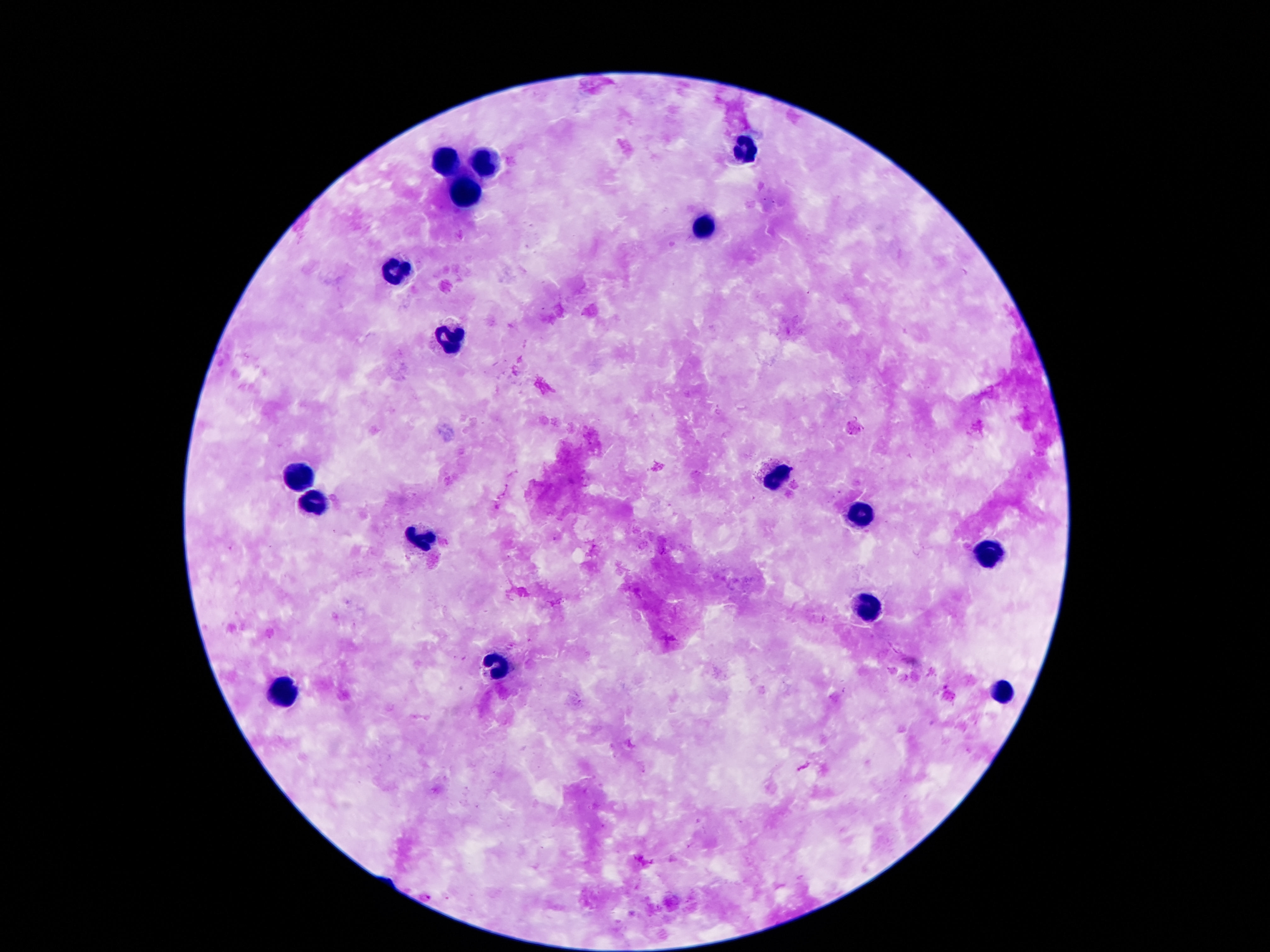

Approximate object centers, in pixels from the top-left corner.
Summary:
  - Leukocyte locations: (x=740, y=150), (x=447, y=162), (x=484, y=162), (x=467, y=193), (x=701, y=229), (x=396, y=268), (x=451, y=337), (x=775, y=474), (x=299, y=477), (x=316, y=505), (x=861, y=513), (x=422, y=539), (x=984, y=554), (x=865, y=608), (x=1002, y=691), (x=281, y=692)
  - Preparation: thick blood smear
  - Magnification: 100x
  - Field of view: single
  - Patient malaria status: not infected
  - Stain: Giemsa
  - Capture: smartphone camera through the microscope eyepiece
  - Image size: 1270×952 pixels